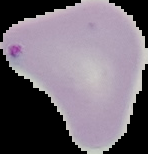

Image is 148×154 pixels. From a thin blood smear. Segmented cell region on a black background. Result: malaria parasites identified.